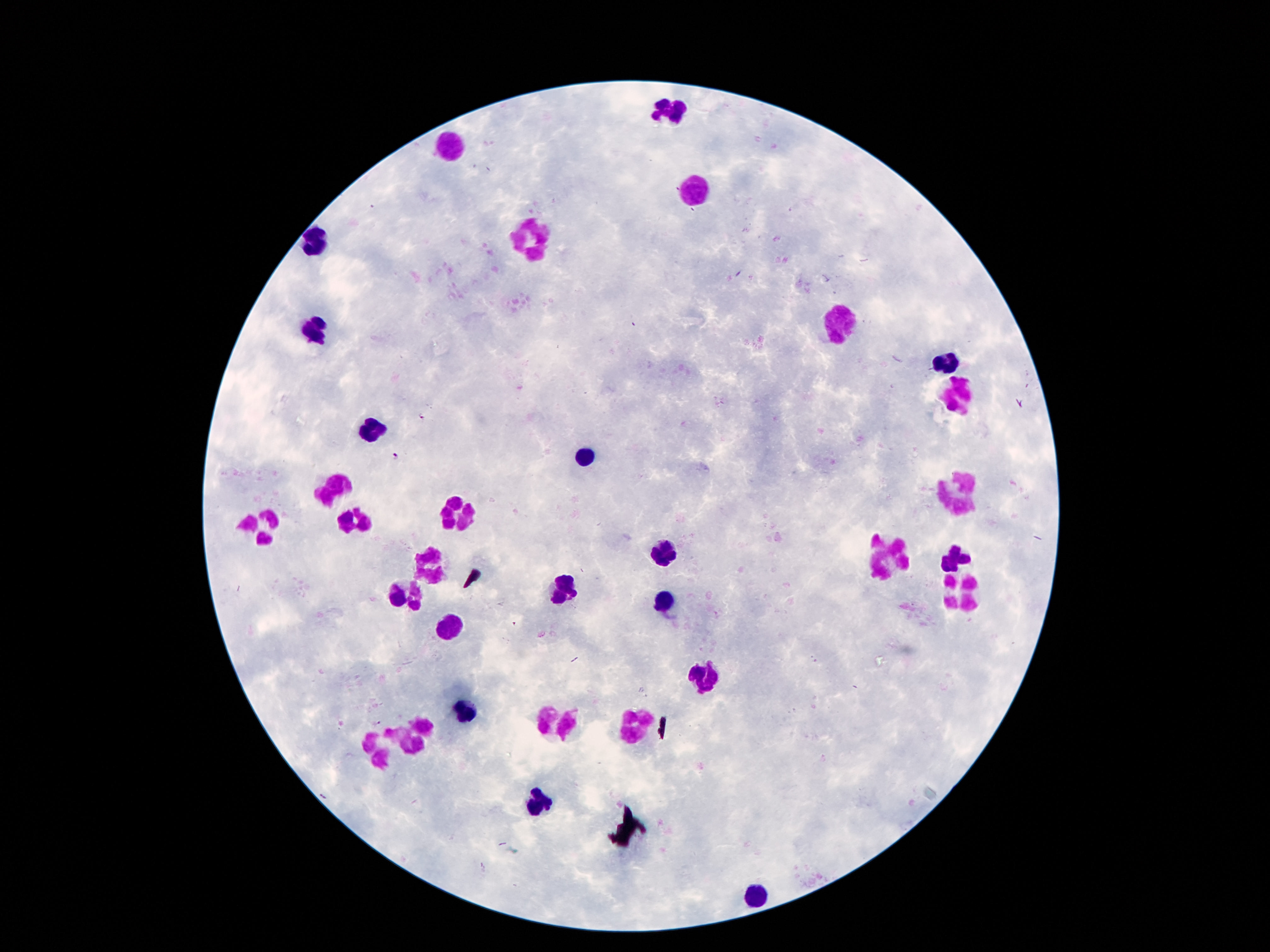
image size = 1270×952 pixels
field of view = one from this slide
patient malaria status = not infected
preparation = thick blood film
stain = Giemsa
magnification = 100x
capture = smartphone camera through the microscope eyepiece
leukocyte locations = approximate centers as {x, y} in pixels: {672, 111}, {453, 145}, {698, 192}, {533, 240}, {315, 244}, {845, 325}, {315, 328}, {946, 365}, {961, 395}, {375, 425}, {586, 453}, {334, 488}, {953, 493}, {459, 513}, {356, 520}, {263, 526}, {664, 554}, {890, 557}, {955, 557}, {431, 563}, {563, 589}, {406, 592}, {963, 592}, {666, 602}, {449, 626}, {703, 678}, {466, 712}, {556, 722}, {634, 725}, {416, 735}, {384, 740}, {541, 800}, {756, 893}